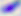
modality: photomicrograph
identification: Toxoplasma gondii
magnification: 400x